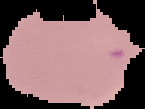

image type = cell region segmented out of the field of view; surrounding area masked to black
image size = 145×109 pixels
malaria status = uninfected
preparation = thin blood film